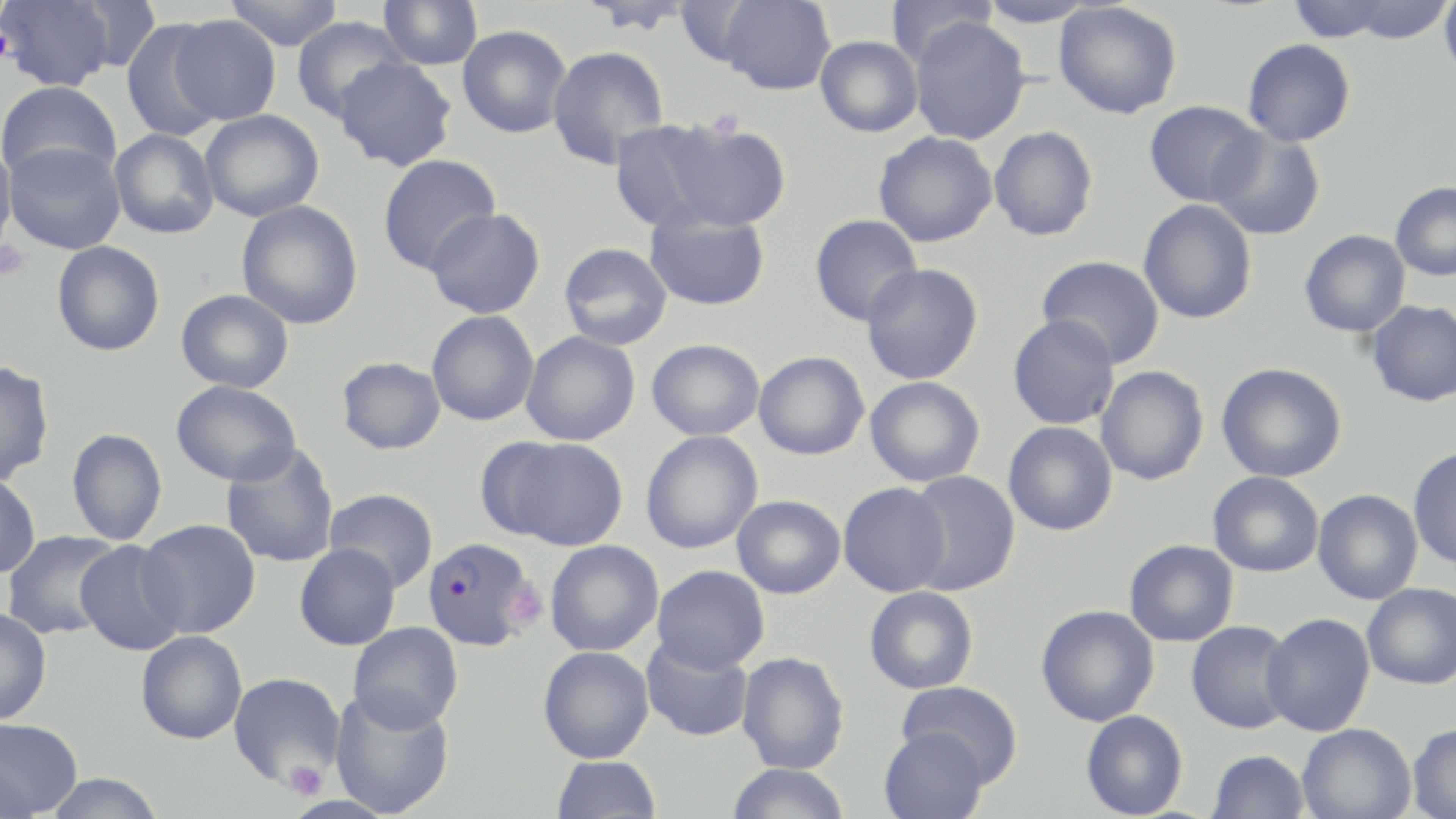

Summary:
  - Coordinate format: approximate bounding boxes as (x1,y1)-(x2,y2) corner pairs in pixels
  - Plasmodium falciparum-infected red blood cell locations: (421,535)-(540,653)
  - Uninfected red blood cell locations: (0,0)-(122,91), (224,0)-(344,50), (378,0)-(483,70), (717,0)-(836,95), (886,0)-(998,69), (978,0)-(1098,28), (1290,0)-(1452,43), (1439,0)-(1456,82), (1053,2)-(1182,119), (169,15)-(280,126), (292,16)-(410,123), (908,18)-(1031,145), (121,19)-(226,142), (458,25)-(572,138), (816,36)-(923,137), (1242,38)-(1356,146), (547,45)-(670,167), (333,57)-(457,172), (0,81)-(122,184), (1144,100)-(1264,207), (199,109)-(325,222), (609,119)-(728,233), (659,120)-(792,231), (989,126)-(1098,241), (1207,127)-(1325,240), (109,129)-(219,239), (873,131)-(998,247), (0,140)-(17,256), (4,141)-(126,254), (377,154)-(501,275), (1391,181)-(1456,281), (1138,199)-(1257,324), (236,200)-(363,330), (644,204)-(771,311), (425,208)-(545,319), (809,214)-(922,326), (1299,229)-(1410,337), (52,241)-(165,356), (559,242)-(673,350), (1036,255)-(1165,369), (861,264)-(983,385), (176,289)-(294,393), (1366,300)-(1456,407), (426,310)-(539,426), (1008,314)-(1120,430), (520,331)-(640,446), (647,339)-(764,441), (753,351)-(870,460), (336,356)-(446,454), (0,360)-(54,486), (1217,362)-(1346,483), (1096,365)-(1209,485), (865,376)-(985,487), (171,380)-(302,486), (1004,421)-(1118,536), (66,429)-(167,545), (641,431)-(763,554), (488,436)-(629,551), (221,442)-(340,568), (1408,444)-(1456,572), (905,471)-(1021,596), (1208,471)-(1324,577), (0,472)-(40,578), (838,482)-(951,596), (324,488)-(438,592), (1313,489)-(1423,604), (732,495)-(845,598), (137,519)-(260,639), (2,530)-(122,640), (74,540)-(187,656), (545,540)-(664,656), (1124,540)-(1238,646), (294,544)-(401,651), (652,564)-(770,672), (1362,583)-(1456,689), (864,586)-(978,694), (1036,604)-(1159,726), (0,608)-(51,724), (1261,612)-(1375,736), (1186,620)-(1298,733), (348,622)-(463,733), (136,631)-(247,744), (640,635)-(754,742), (538,646)-(654,763), (737,651)-(850,774), (228,672)-(345,788), (896,681)-(1023,784), (329,689)-(455,817), (1081,710)-(1188,818), (0,718)-(82,817), (1297,722)-(1416,819), (1408,723)-(1456,818), (879,727)-(989,819), (1207,749)-(1310,819), (550,755)-(662,818), (725,763)-(851,819), (42,773)-(167,819)
  - Platelet locations: (0,23)-(15,70), (708,109)-(744,137), (0,241)-(29,282), (503,580)-(547,630), (283,760)-(328,800)
  - Slide-level diagnosis: Plasmodium falciparum
  - Image size: 1456×819 pixels
  - Magnification: 1000x
  - Modality: optical microscopy
  - Stain: May-Grünwald-Giemsa
  - Field of view: one of a larger specimen
  - Preparation: thin blood smear